Locate and identify every blood parasite.
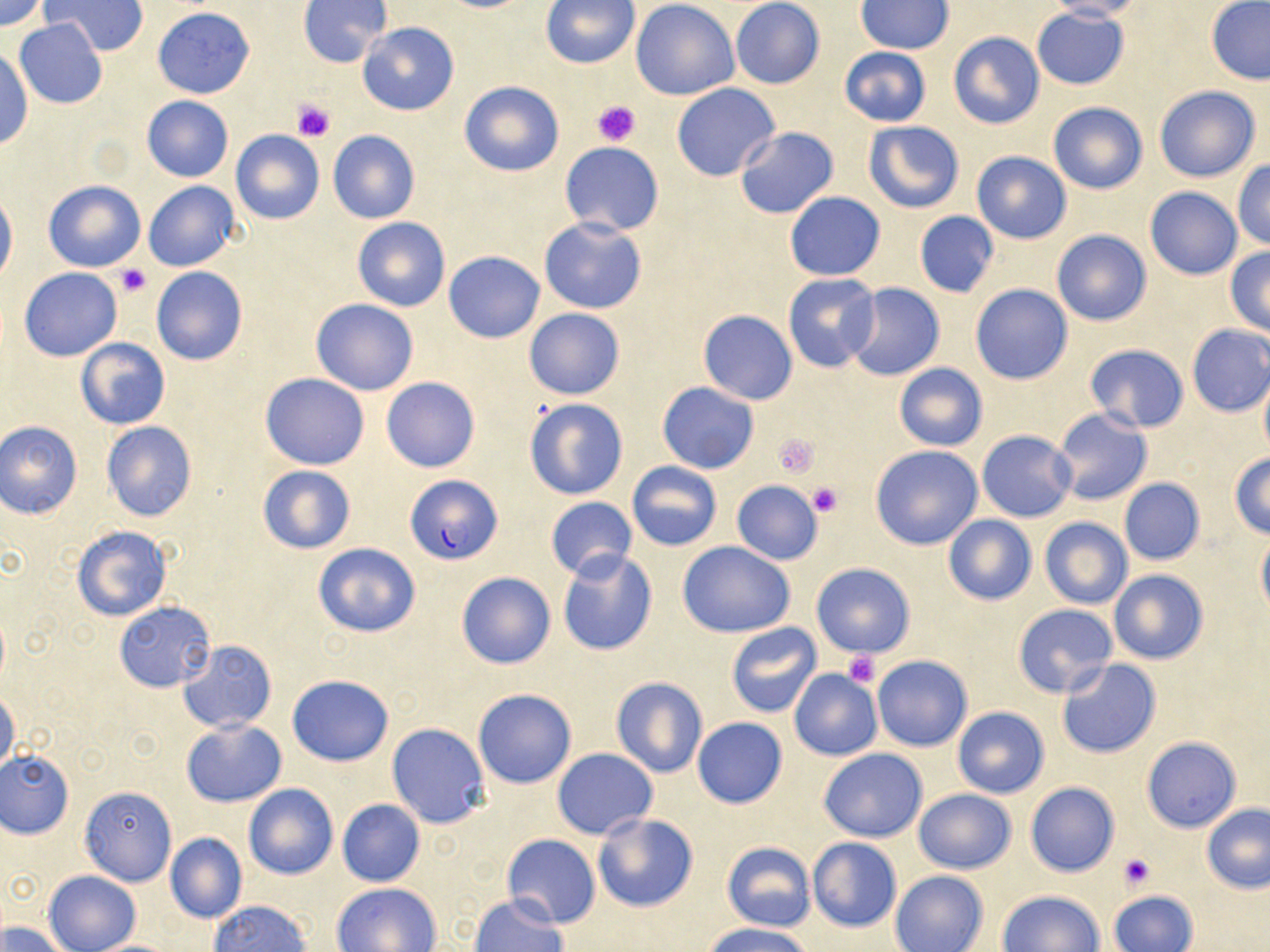
Approximate bounding boxes as named x1/y1/x2/y2 corners in pixels.
Plasmodium falciparum-infected red blood cells: (x1=404, y1=475, x2=502, y2=566).
No Plasmodium ovale, Plasmodium malariae, Plasmodium vivax, Babesia divergens, or Trypanosoma brucei observed.

slide-level diagnosis = Plasmodium falciparum
image size = 1270×952 pixels
preparation = thin blood smear
modality = optical microscopy
stain = May-Grünwald-Giemsa
magnification = 1000x
uninfected red blood cell locations = approximate bounding boxes as named x1/y1/x2/y2 corners in pixels: (x1=1, y1=0, x2=48, y2=31), (x1=297, y1=0, x2=392, y2=68), (x1=731, y1=0, x2=825, y2=89), (x1=1042, y1=0, x2=1145, y2=21), (x1=44, y1=1, x2=146, y2=56), (x1=541, y1=1, x2=641, y2=70), (x1=631, y1=1, x2=740, y2=101), (x1=857, y1=1, x2=954, y2=54), (x1=1205, y1=1, x2=1270, y2=85), (x1=153, y1=6, x2=254, y2=99), (x1=1033, y1=8, x2=1129, y2=90), (x1=15, y1=19, x2=108, y2=108), (x1=358, y1=22, x2=459, y2=116), (x1=948, y1=32, x2=1044, y2=129), (x1=838, y1=47, x2=932, y2=127), (x1=1, y1=48, x2=32, y2=150), (x1=458, y1=80, x2=565, y2=177), (x1=671, y1=82, x2=781, y2=182), (x1=1153, y1=84, x2=1263, y2=183), (x1=142, y1=96, x2=233, y2=182), (x1=1047, y1=101, x2=1149, y2=195), (x1=863, y1=121, x2=965, y2=214), (x1=733, y1=127, x2=839, y2=218), (x1=230, y1=131, x2=325, y2=225), (x1=327, y1=131, x2=421, y2=224), (x1=560, y1=143, x2=665, y2=235), (x1=971, y1=151, x2=1072, y2=244), (x1=1232, y1=159, x2=1270, y2=251), (x1=43, y1=179, x2=147, y2=272), (x1=144, y1=179, x2=242, y2=272), (x1=1144, y1=187, x2=1243, y2=280), (x1=0, y1=188, x2=17, y2=288), (x1=783, y1=192, x2=886, y2=280), (x1=914, y1=212, x2=999, y2=297), (x1=539, y1=217, x2=646, y2=314), (x1=353, y1=218, x2=450, y2=312), (x1=1051, y1=230, x2=1150, y2=327), (x1=1224, y1=247, x2=1270, y2=336), (x1=444, y1=252, x2=544, y2=343), (x1=151, y1=267, x2=248, y2=366), (x1=18, y1=268, x2=122, y2=360), (x1=782, y1=273, x2=880, y2=373), (x1=847, y1=284, x2=945, y2=381), (x1=970, y1=284, x2=1072, y2=385), (x1=310, y1=299, x2=419, y2=396), (x1=523, y1=308, x2=625, y2=401), (x1=698, y1=310, x2=798, y2=405), (x1=1186, y1=325, x2=1270, y2=416), (x1=75, y1=338, x2=171, y2=430), (x1=1083, y1=343, x2=1189, y2=432), (x1=893, y1=362, x2=989, y2=452), (x1=260, y1=373, x2=370, y2=470), (x1=1258, y1=373, x2=1270, y2=458), (x1=381, y1=377, x2=480, y2=473), (x1=657, y1=382, x2=759, y2=473), (x1=523, y1=397, x2=628, y2=500), (x1=1052, y1=409, x2=1152, y2=506), (x1=1, y1=421, x2=83, y2=519), (x1=101, y1=421, x2=198, y2=522), (x1=976, y1=430, x2=1077, y2=522), (x1=869, y1=445, x2=983, y2=550), (x1=1228, y1=453, x2=1270, y2=539), (x1=626, y1=462, x2=722, y2=550), (x1=257, y1=466, x2=355, y2=553), (x1=1118, y1=478, x2=1205, y2=565), (x1=731, y1=481, x2=824, y2=564), (x1=545, y1=498, x2=639, y2=579), (x1=942, y1=515, x2=1038, y2=605), (x1=1040, y1=517, x2=1132, y2=609), (x1=71, y1=524, x2=173, y2=623), (x1=1255, y1=532, x2=1270, y2=620), (x1=677, y1=542, x2=797, y2=638), (x1=312, y1=543, x2=420, y2=637), (x1=557, y1=550, x2=657, y2=657), (x1=810, y1=562, x2=916, y2=658), (x1=1109, y1=569, x2=1209, y2=664), (x1=455, y1=572, x2=555, y2=670), (x1=115, y1=602, x2=216, y2=691), (x1=1013, y1=604, x2=1117, y2=697), (x1=726, y1=622, x2=822, y2=717), (x1=179, y1=640, x2=276, y2=733), (x1=872, y1=654, x2=973, y2=752), (x1=1054, y1=659, x2=1162, y2=760), (x1=788, y1=669, x2=882, y2=761), (x1=286, y1=674, x2=393, y2=766), (x1=610, y1=676, x2=708, y2=778), (x1=473, y1=688, x2=578, y2=789), (x1=0, y1=689, x2=20, y2=776), (x1=951, y1=706, x2=1050, y2=798), (x1=691, y1=717, x2=788, y2=808), (x1=182, y1=718, x2=286, y2=807), (x1=386, y1=722, x2=490, y2=828), (x1=1141, y1=737, x2=1242, y2=833), (x1=819, y1=748, x2=928, y2=842), (x1=552, y1=749, x2=657, y2=838), (x1=0, y1=750, x2=74, y2=839), (x1=1023, y1=782, x2=1120, y2=877), (x1=243, y1=783, x2=338, y2=880), (x1=78, y1=786, x2=177, y2=884), (x1=912, y1=788, x2=1016, y2=874), (x1=337, y1=799, x2=425, y2=887), (x1=1200, y1=803, x2=1270, y2=894), (x1=591, y1=812, x2=699, y2=913), (x1=165, y1=832, x2=247, y2=924), (x1=501, y1=835, x2=600, y2=928), (x1=806, y1=837, x2=903, y2=932), (x1=720, y1=841, x2=817, y2=932), (x1=43, y1=870, x2=141, y2=952), (x1=889, y1=871, x2=989, y2=952), (x1=332, y1=882, x2=443, y2=951), (x1=997, y1=890, x2=1106, y2=952), (x1=1109, y1=890, x2=1199, y2=952), (x1=468, y1=893, x2=568, y2=952), (x1=209, y1=900, x2=312, y2=951), (x1=0, y1=921, x2=68, y2=952), (x1=703, y1=923, x2=815, y2=952), (x1=86, y1=939, x2=182, y2=951)
platelet locations = approximate bounding boxes as named x1/y1/x2/y2 corners in pixels: (x1=291, y1=98, x2=336, y2=141), (x1=592, y1=100, x2=640, y2=146), (x1=113, y1=264, x2=151, y2=298), (x1=773, y1=434, x2=819, y2=478), (x1=807, y1=481, x2=844, y2=518), (x1=842, y1=650, x2=881, y2=689), (x1=1119, y1=853, x2=1155, y2=889)
field of view = single